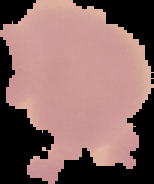
Summary:
  - Malaria status: uninfected
  - Image type: segmented cell region with the area outside set to black
  - Image size: 154×184 pixels
  - Preparation: thin blood film